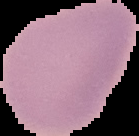
malaria status = uninfected
image type = cell region segmented out of the field of view; surrounding area masked to black
image size = 139×136 pixels
preparation = thin blood smear